Classify the preparation.
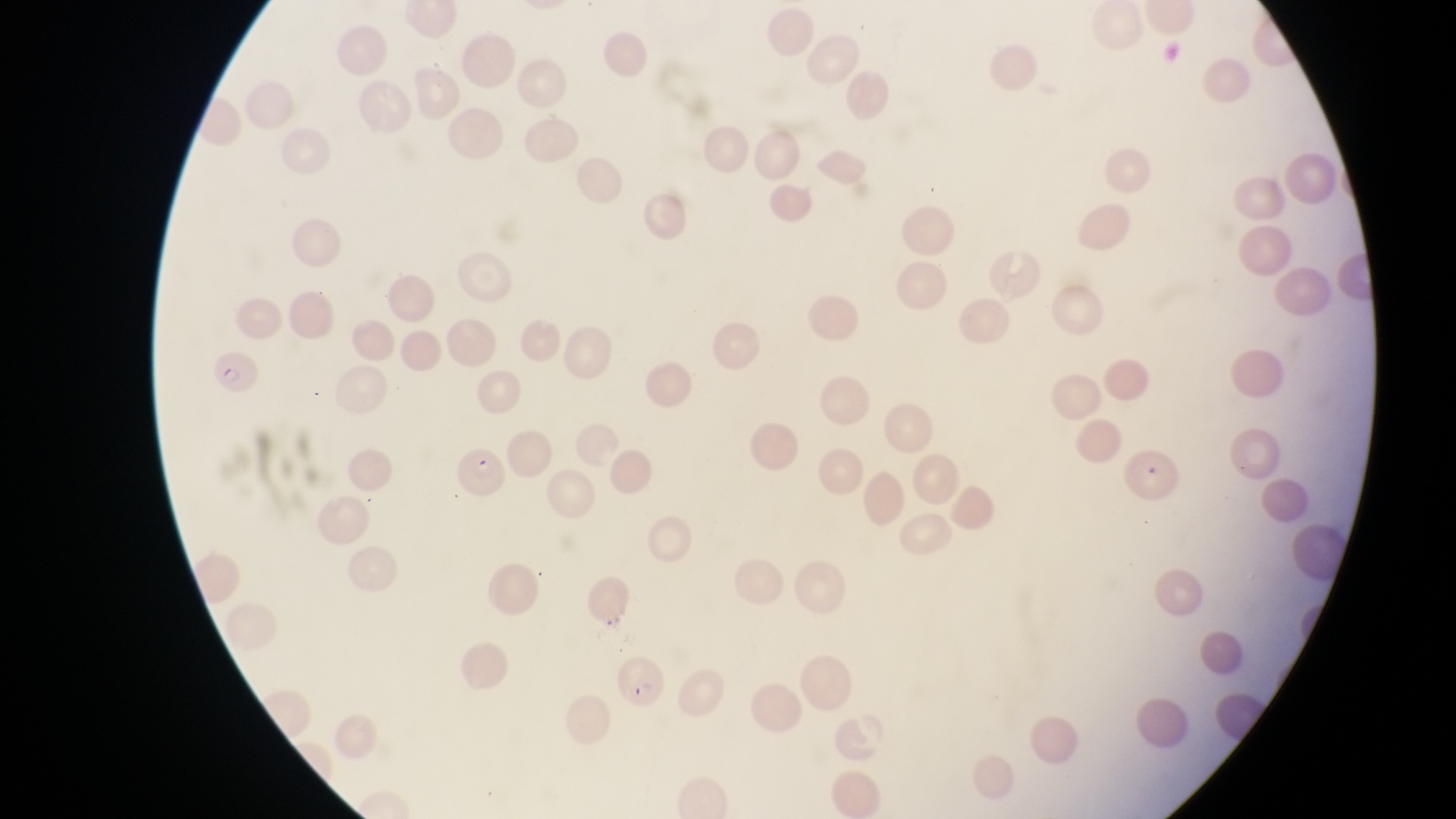
Thin blood film.

magnification: 1000x
image_size: 1456×819 pixels
parasitised_red_blood_cell_locations: 'approximate bounding boxes as left top right bottom in pixels: 212 354 261 401; 452 444 508 499; 1125 447 1189 519; 617 655 666 713'
field_of_view: single
capture: smartphone photograph through the eyepiece of an Olympus CX-23 microscope
country: Uganda